State the blood parasite species.
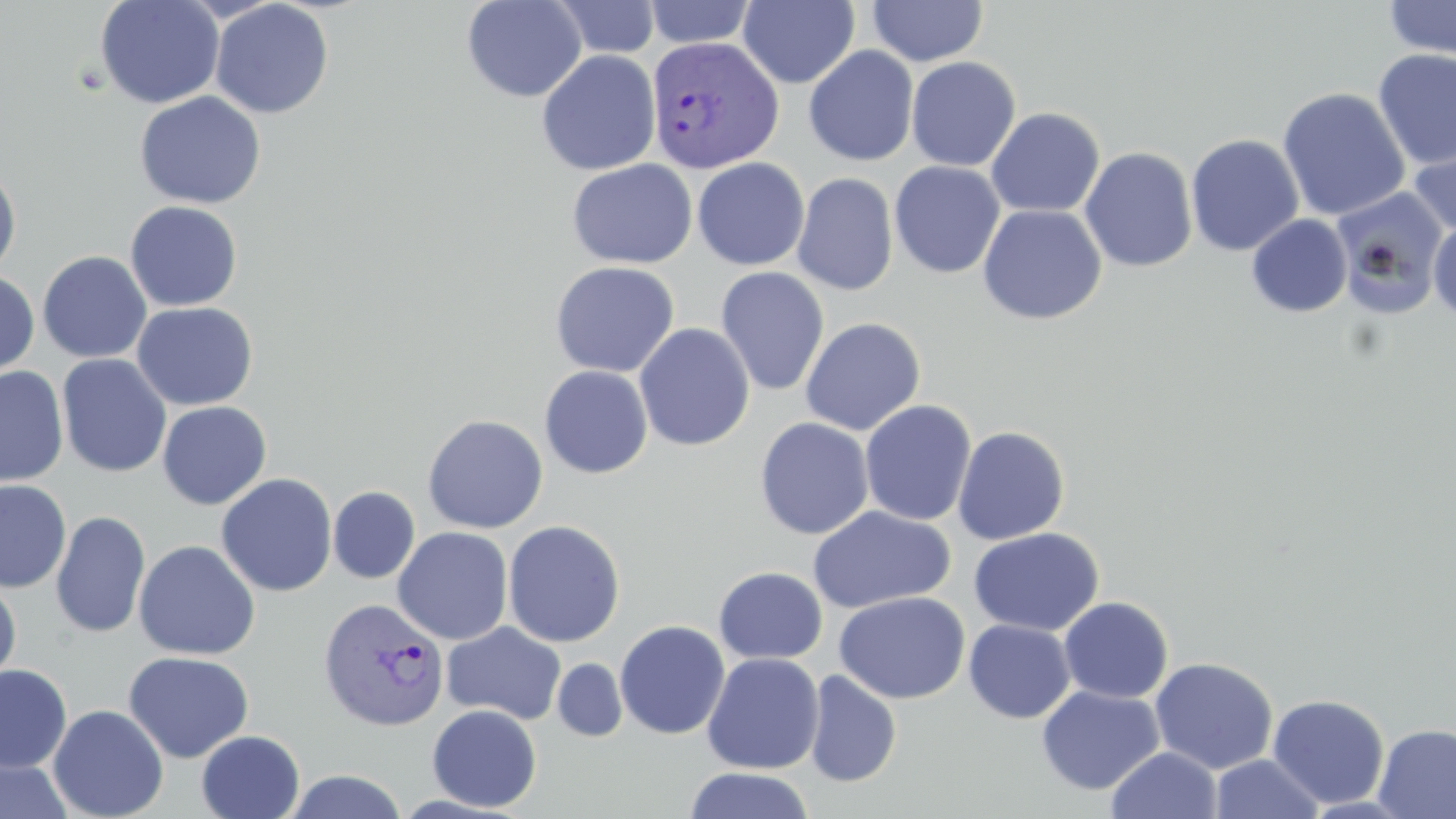

Plasmodium vivax.

Summary:
  - Coordinate format: approximate bounding boxes as (x1, y1, x2, y2) in pixels
  - Uninfected red blood cell locations: (95, 0, 225, 110), (462, 0, 586, 103), (549, 0, 662, 60), (738, 0, 860, 88), (867, 0, 988, 66), (1384, 0, 1455, 61), (210, 1, 334, 119), (643, 1, 756, 49), (803, 46, 919, 166), (1372, 48, 1456, 171), (537, 50, 661, 176), (906, 56, 1021, 172), (1277, 87, 1411, 222), (134, 91, 266, 209), (985, 107, 1105, 218), (1407, 132, 1456, 240), (1185, 133, 1304, 256), (1079, 147, 1198, 272), (692, 157, 810, 271), (566, 158, 698, 269), (889, 161, 1006, 279), (0, 162, 22, 278), (792, 172, 898, 296), (1331, 188, 1449, 320), (125, 200, 243, 312), (977, 204, 1107, 325), (1246, 214, 1352, 318), (1428, 220, 1456, 323), (38, 251, 152, 364), (549, 260, 680, 377), (715, 266, 830, 397), (0, 269, 40, 381), (131, 301, 259, 411), (799, 317, 926, 436), (634, 323, 755, 452), (57, 354, 172, 478), (539, 365, 653, 479), (0, 366, 69, 488), (859, 399, 976, 526), (156, 401, 272, 510), (422, 414, 548, 533), (754, 417, 875, 540), (952, 425, 1071, 545), (216, 473, 338, 597), (0, 480, 71, 592), (328, 486, 420, 584), (807, 506, 957, 614), (51, 511, 150, 638), (503, 519, 625, 648), (393, 526, 513, 645), (968, 527, 1104, 636), (134, 540, 261, 660), (713, 566, 828, 664), (0, 574, 22, 691), (834, 591, 970, 703), (1058, 596, 1173, 704), (964, 619, 1076, 723), (614, 620, 730, 740), (441, 622, 567, 725), (123, 651, 254, 763), (702, 652, 824, 774), (1149, 657, 1279, 774), (552, 658, 627, 742), (1, 664, 71, 772), (803, 670, 902, 788), (1036, 685, 1165, 795), (1267, 693, 1390, 809), (48, 704, 168, 819), (427, 704, 542, 813), (1373, 723, 1456, 819), (196, 730, 305, 818), (1106, 747, 1222, 819), (1209, 753, 1326, 818), (0, 757, 74, 819), (684, 767, 815, 819), (284, 769, 408, 818)
  - Plasmodium vivax-infected red blood cell locations: (645, 36, 784, 175), (318, 597, 449, 731)
  - Magnification: 1000x
  - Preparation: thin blood smear
  - Stain: May-Grünwald-Giemsa
  - Field of view: one of a larger specimen
  - Image size: 1456×819 pixels
  - Modality: optical microscopy